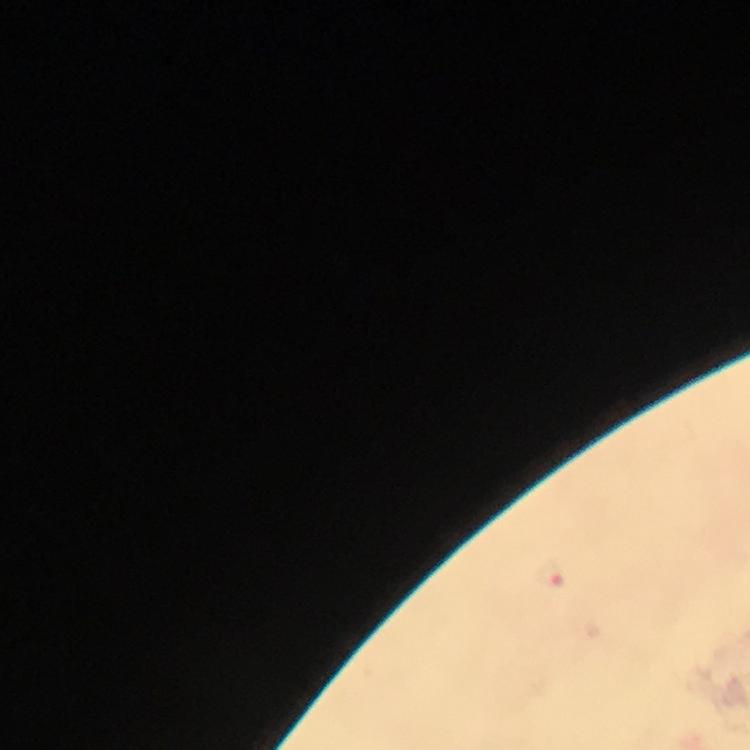
Approximate centers as {x, y} in pixels. Plasmodium parasite locations: {548, 574}. Cropped region of a single field of view. Thick blood film. Giemsa-stained preparation. Immersion oil was used. From a malaria diagnostic workup. At 100x magnification. Image is 750×750 pixels. Photographed with a smartphone mounted on the microscope.